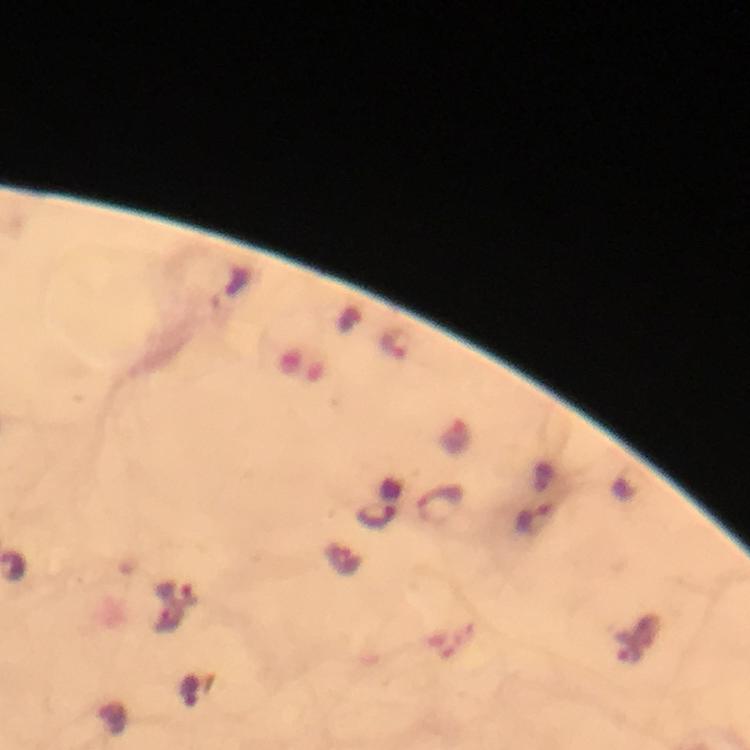
malaria parasite locations = approximate object centers, in pixels from the top-left corner: (x=398, y=344), (x=445, y=504), (x=378, y=517), (x=537, y=518), (x=178, y=595), (x=628, y=650)
cropped from = a single field of view
image size = 750×750 pixels
immersion oil = used
stain = Giemsa
preparation = thick blood film
magnification = 100x
capture = smartphone mounted on the microscope
context = from a malaria diagnostic workup